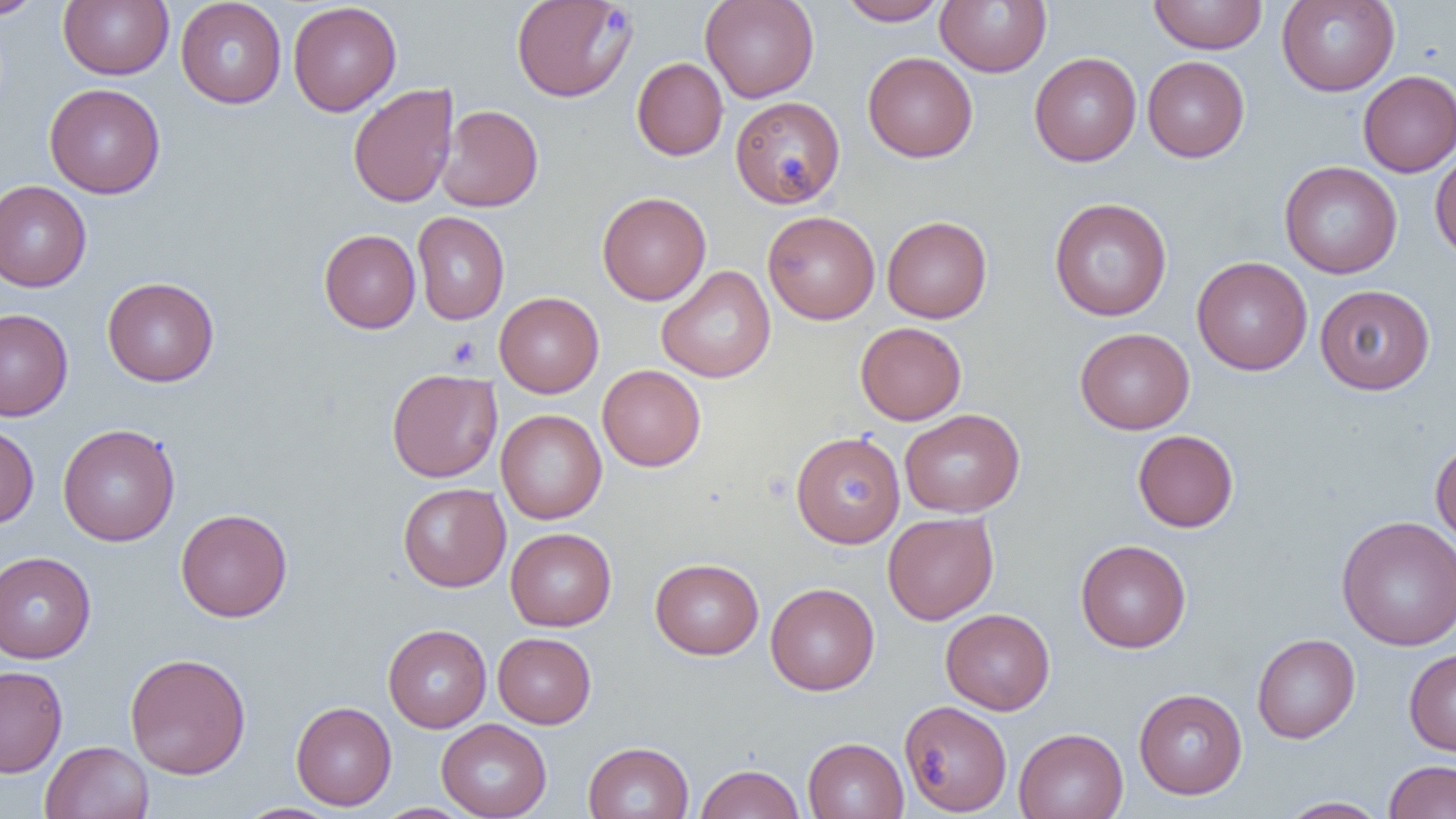
Approximate bounding boxes as [x1, y1, x2, y2] in pixels. Platelet locations: [447, 336, 481, 368]. Uninfected red blood cell locations: [1, 0, 45, 20], [59, 0, 174, 80], [511, 0, 637, 102], [700, 0, 819, 103], [838, 0, 947, 26], [935, 0, 1051, 77], [1148, 0, 1268, 54], [1276, 0, 1400, 96], [175, 1, 287, 108], [287, 1, 401, 116], [863, 52, 978, 162], [1029, 52, 1141, 166], [1142, 56, 1249, 162], [632, 57, 728, 161], [1358, 70, 1456, 177], [44, 83, 165, 199], [347, 83, 458, 208], [730, 96, 845, 208], [437, 105, 543, 212], [1429, 145, 1456, 261], [1279, 161, 1402, 279], [0, 180, 91, 292], [597, 191, 711, 305], [1049, 197, 1172, 321], [412, 211, 509, 325], [762, 211, 880, 324], [882, 215, 992, 323], [319, 229, 420, 333], [1192, 256, 1313, 375], [656, 265, 776, 383], [102, 277, 219, 387], [1314, 284, 1435, 395], [494, 292, 604, 397], [0, 308, 73, 421], [855, 322, 967, 425], [1075, 328, 1195, 434], [597, 365, 706, 471], [386, 369, 502, 482], [496, 409, 607, 524], [900, 409, 1024, 517], [57, 423, 180, 546], [0, 424, 39, 529], [1132, 429, 1239, 532], [790, 431, 905, 548], [1430, 440, 1456, 551], [397, 482, 510, 592], [176, 508, 293, 622], [883, 511, 999, 625], [1336, 515, 1456, 651], [506, 527, 616, 631], [1075, 539, 1191, 653], [0, 551, 96, 663], [650, 558, 764, 659], [766, 582, 879, 695], [940, 608, 1055, 714], [383, 624, 491, 732], [493, 632, 596, 728], [1252, 633, 1360, 743], [1404, 648, 1456, 756], [124, 652, 251, 779], [0, 665, 68, 777], [1133, 688, 1248, 799], [899, 700, 1012, 815], [291, 701, 396, 810], [436, 718, 552, 819], [1014, 728, 1128, 819], [802, 737, 908, 819], [40, 740, 154, 819], [583, 741, 694, 819], [1384, 760, 1456, 818], [694, 763, 805, 819], [1279, 797, 1390, 818], [234, 803, 343, 819], [373, 804, 475, 819]. Slide-level diagnosis: negative for blood parasites. Thin blood smear. Image is 1456×819 pixels. Optical microscopy. Single field of view. Captured at 1000x magnification.